Locate every blood parasite and identify its species.
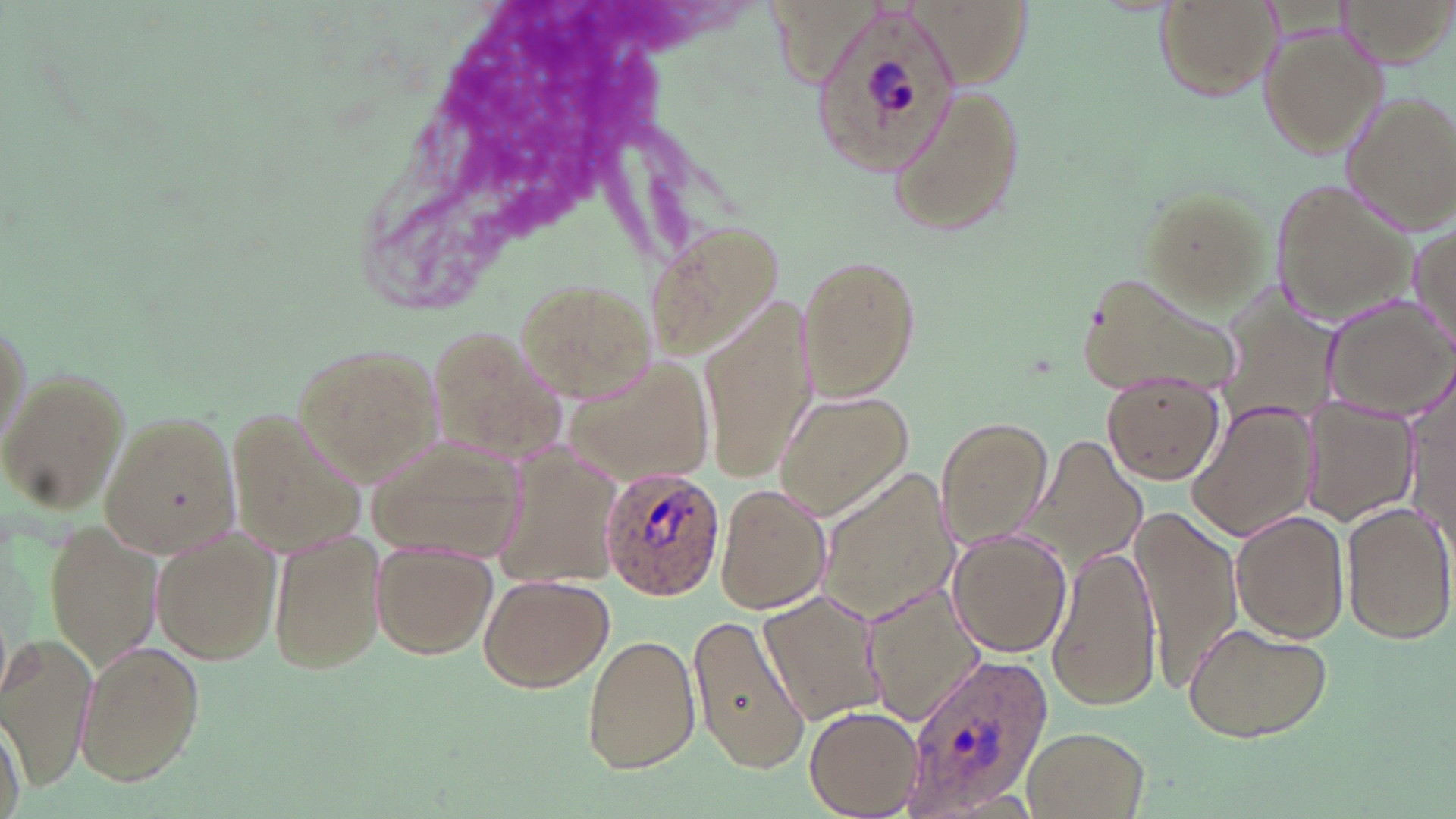
Approximate bounding boxes as [x1, y1, x2, y2] in pixels.
Plasmodium ovale-infected red blood cells: [811, 3, 961, 178], [598, 465, 723, 599], [901, 651, 1054, 811].
No Plasmodium falciparum, Plasmodium malariae, Plasmodium vivax, Babesia divergens, or Trypanosoma brucei observed.

Uninfected red blood cell locations: [1339, 0, 1452, 67], [1154, 1, 1277, 104], [1256, 22, 1389, 160], [884, 80, 1026, 238], [1339, 88, 1456, 232], [1269, 175, 1419, 329], [1138, 182, 1277, 313], [1407, 221, 1456, 354], [641, 222, 783, 369], [795, 252, 923, 402], [1075, 267, 1245, 401], [1211, 272, 1345, 441], [521, 279, 659, 404], [703, 290, 817, 486], [1323, 298, 1455, 421], [0, 303, 34, 457], [427, 323, 576, 474], [295, 343, 446, 485], [560, 351, 723, 491], [1, 367, 129, 511], [1405, 369, 1455, 550], [1103, 373, 1222, 484], [776, 390, 915, 519], [1301, 395, 1418, 526], [1187, 398, 1314, 540], [224, 405, 366, 566], [97, 410, 238, 557], [935, 416, 1052, 546], [1206, 420, 1332, 633], [1031, 433, 1148, 567], [493, 435, 622, 591], [368, 442, 528, 561], [817, 471, 961, 620], [715, 484, 832, 614], [1341, 500, 1455, 645], [1229, 509, 1350, 644], [1131, 510, 1243, 688], [45, 521, 165, 674], [150, 527, 281, 664], [270, 528, 387, 677], [946, 528, 1072, 656], [370, 543, 498, 659], [1048, 544, 1162, 710], [476, 573, 615, 694], [862, 581, 989, 724], [759, 586, 890, 725], [686, 613, 812, 776], [1180, 621, 1335, 742], [582, 632, 701, 773], [2, 635, 97, 787], [72, 639, 206, 788], [806, 705, 921, 816], [2, 708, 26, 819], [1022, 726, 1149, 818]. Slide-level diagnosis: Plasmodium ovale. Thin blood film. Single field of view. Light microscopy. Captured at 1000x magnification. Image is 1456×819 pixels. May-Grünwald-Giemsa-stained preparation.